Describe the morphology of the erythrocytes.
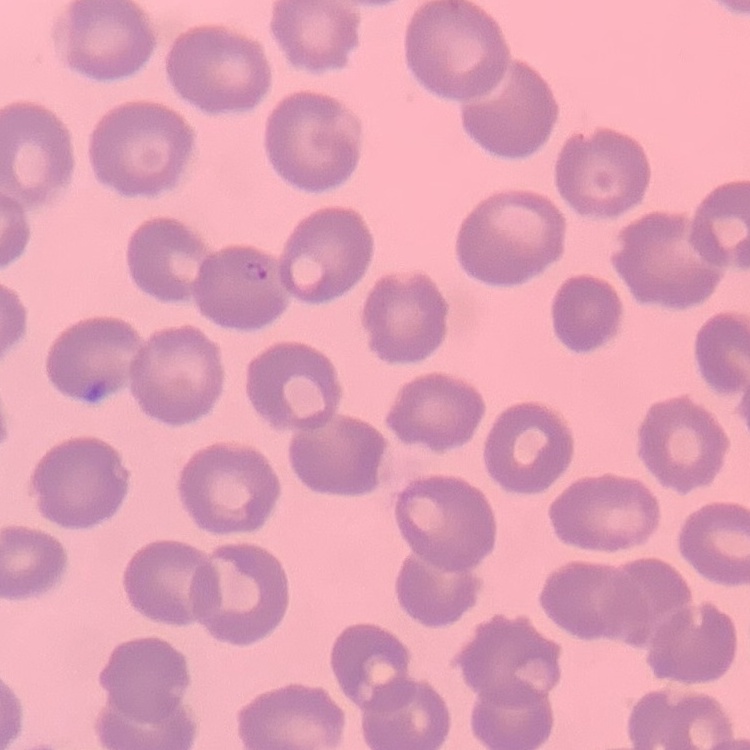

They show no rouleaux formation.

Square crop of a larger photomicrograph. Field's or Giemsa stain. Thin blood film.